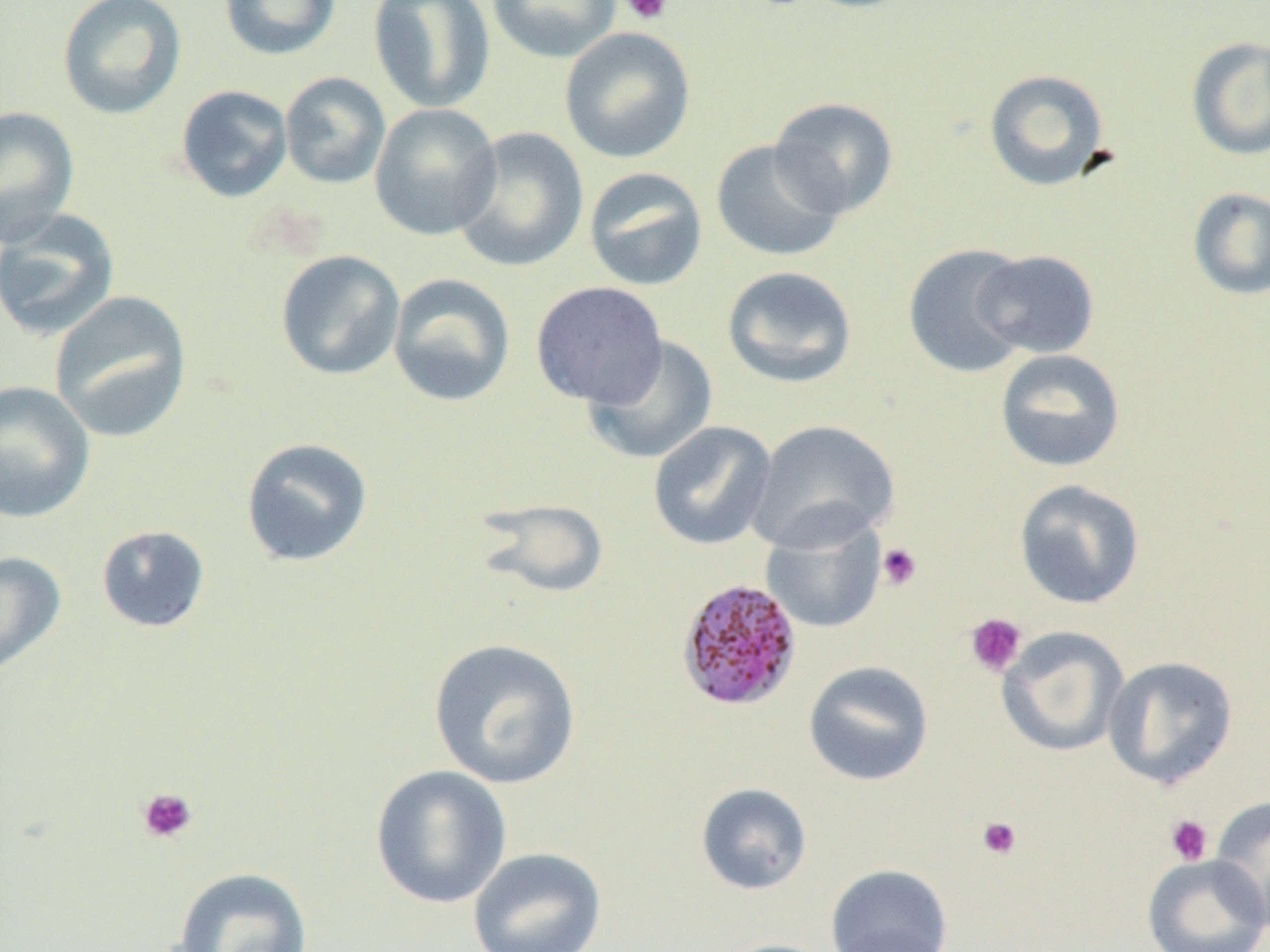
Approximate bounding boxes as [x1, y1, x2, y2] in pixels. Plasmodium malariae-infected red blood cell locations: [676, 578, 803, 712]. Uninfected red blood cell locations: [57, 0, 187, 120], [219, 0, 342, 61], [368, 0, 496, 114], [486, 0, 621, 63], [559, 26, 696, 164], [1186, 37, 1270, 161], [983, 68, 1111, 191], [279, 72, 391, 189], [175, 84, 294, 204], [769, 97, 899, 219], [369, 103, 502, 240], [0, 107, 80, 247], [450, 126, 588, 273], [711, 139, 846, 262], [583, 167, 708, 292], [1187, 186, 1270, 300], [0, 207, 121, 341], [903, 243, 1034, 378], [973, 249, 1100, 359], [275, 250, 405, 381], [721, 265, 857, 388], [387, 273, 516, 408], [530, 281, 668, 408], [49, 291, 193, 442], [582, 335, 719, 465], [995, 349, 1126, 473], [0, 381, 96, 523], [747, 419, 900, 552], [648, 421, 777, 551], [240, 437, 374, 568], [1014, 478, 1146, 610], [471, 497, 610, 600], [760, 511, 888, 634], [96, 525, 211, 633], [0, 551, 67, 676], [996, 626, 1129, 758], [427, 638, 582, 790], [1102, 655, 1239, 790], [802, 660, 934, 787], [370, 765, 512, 909], [695, 783, 813, 895], [1210, 795, 1270, 933], [467, 847, 607, 952], [1142, 854, 1269, 952], [825, 864, 953, 952], [172, 866, 314, 952], [825, 924, 955, 952], [713, 938, 839, 952]. Platelet locations: [620, 0, 672, 25], [877, 543, 922, 591], [965, 613, 1027, 677], [136, 787, 199, 844], [1165, 814, 1214, 866], [977, 816, 1023, 860]. Slide-level diagnosis: Plasmodium malariae. One field of a larger specimen. Light microscopy. Thin blood film. Image is 1270×952 pixels. Captured at 1000x magnification.